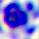
{
  "magnification": "400x",
  "identification": "white blood cell",
  "modality": "micrograph"
}